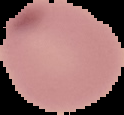 From a thin blood smear. Cell region segmented out of the field of view; the surrounding area is masked to black. Image is 124×115 pixels. Result: no malaria parasites detected.